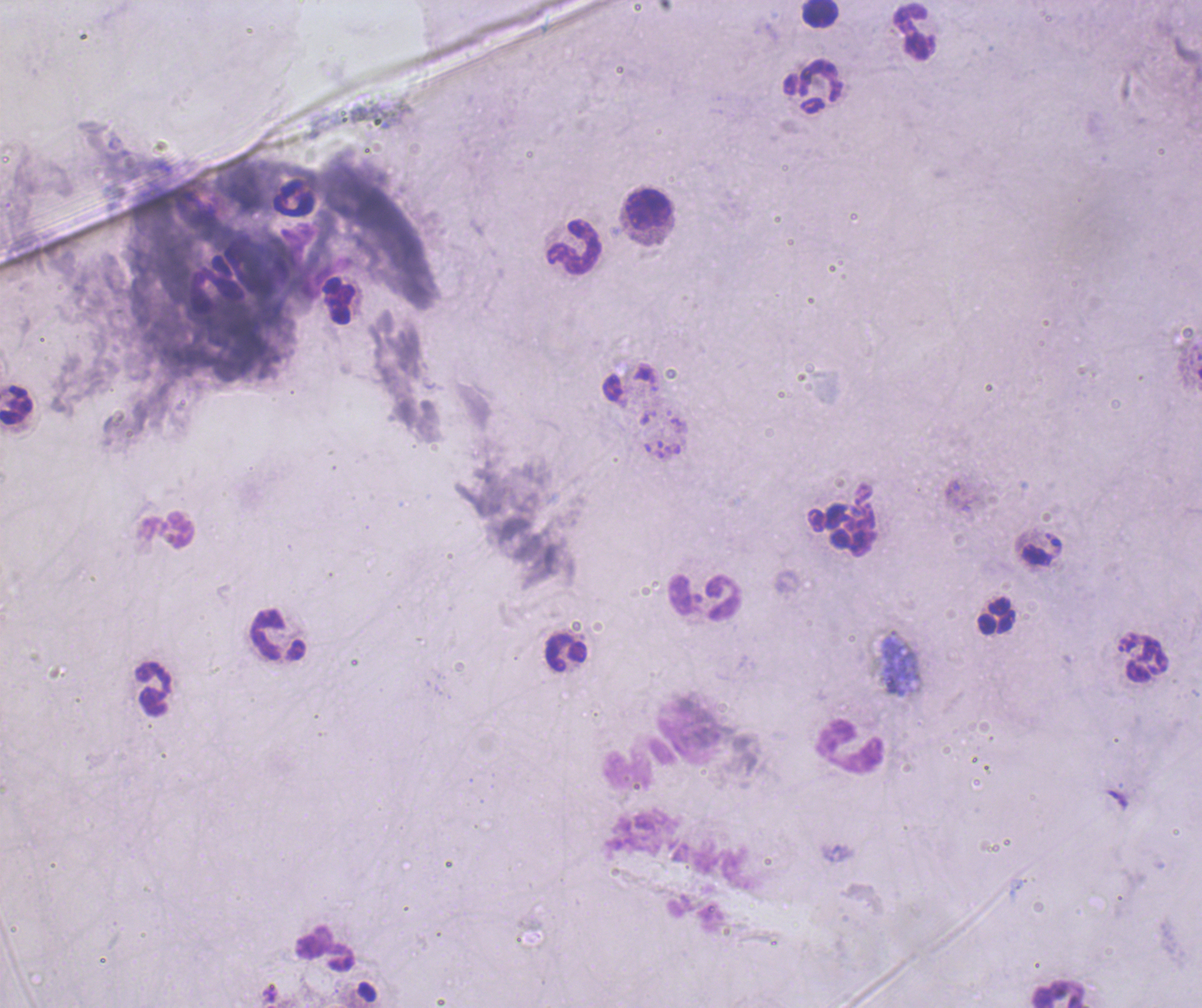

coordinate format = approximate centers as {x, y} in pixels
leukocyte locations = {819, 13}, {913, 31}, {811, 86}, {295, 198}, {647, 210}, {574, 246}, {340, 302}, {16, 405}, {164, 532}, {706, 596}, {995, 616}, {278, 634}, {565, 651}, {1143, 657}, {153, 688}, {848, 746}, {638, 764}, {325, 950}, {1059, 993}
coloration quality = bad
image size = 1202×1008 pixels
background quality = poor
result = no Plasmodium parasites detected
magnification = 100x
stain = Romanowsky
preparation = thick smear of blood
context = previously used in an actual diagnosis
field of view = one from this slide